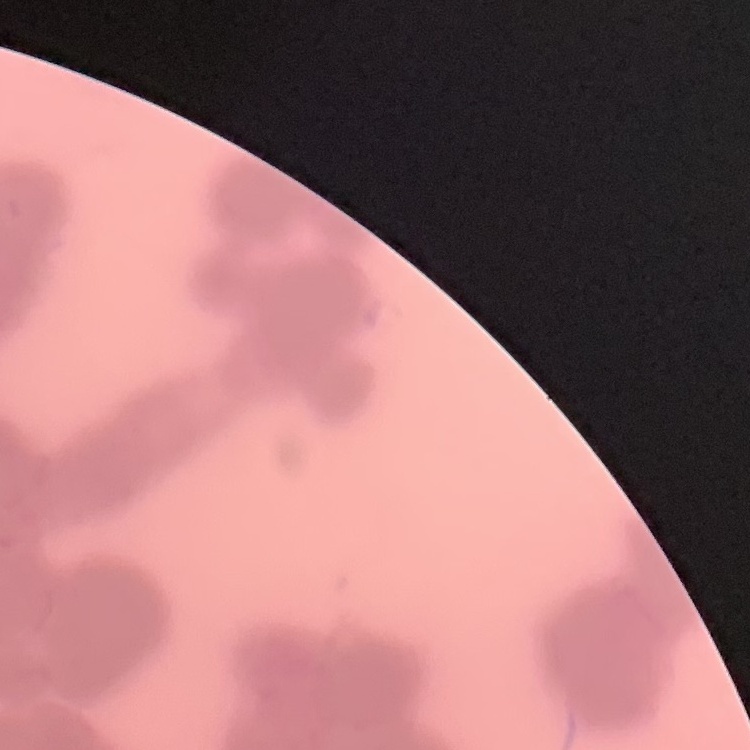

The red blood cells show rouleaux formation. Thin blood film. Field's or Giemsa stain. Square crop of a larger photomicrograph.